State the blood parasite species.
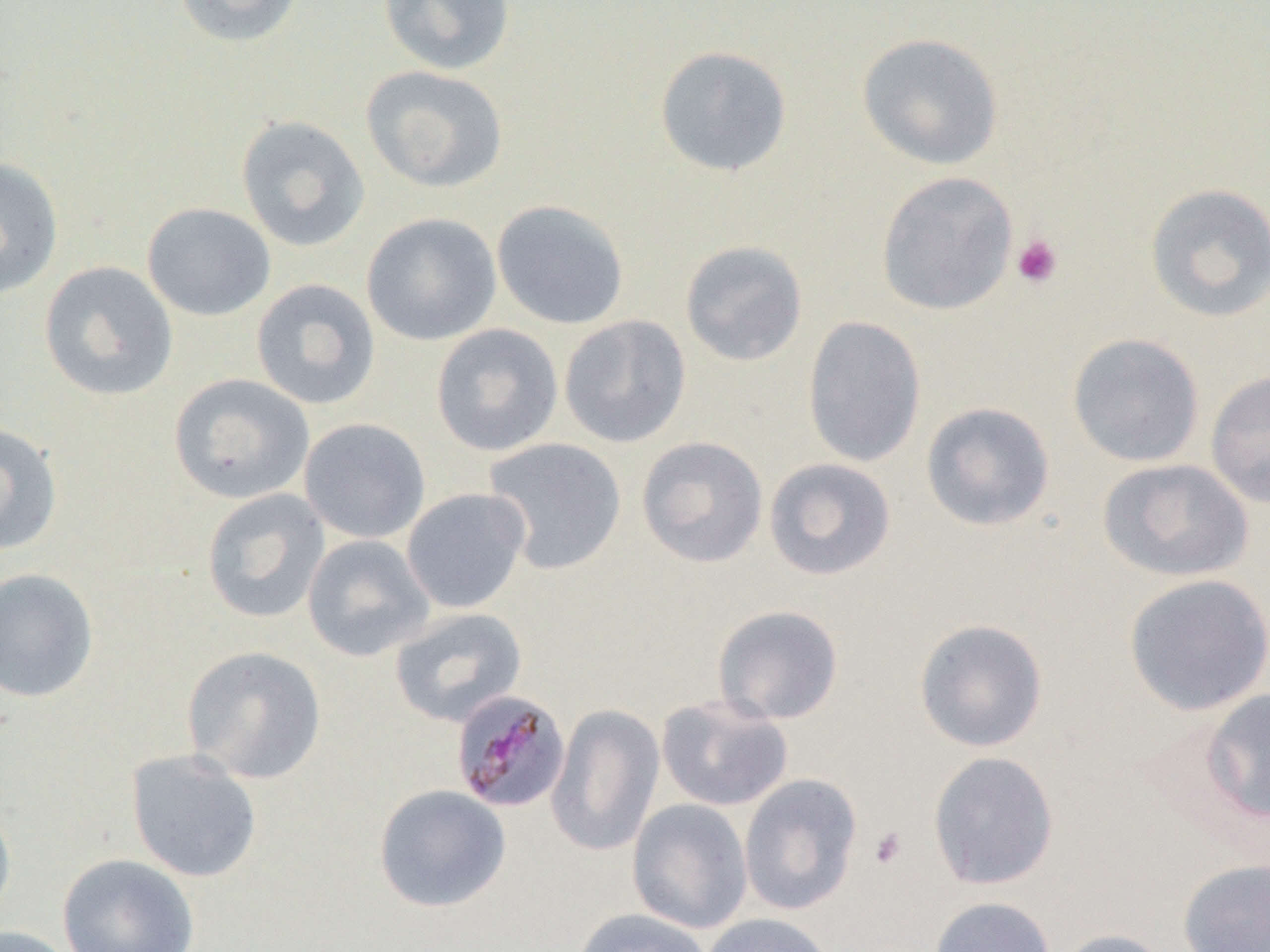
Plasmodium malariae.

Approximate bounding boxes as [x1, y1, x2, y2] in pixels. Uninfected red blood cell locations: [172, 0, 305, 48], [378, 0, 516, 75], [856, 32, 1004, 170], [654, 45, 793, 177], [361, 65, 509, 193], [235, 115, 371, 253], [0, 157, 64, 299], [876, 171, 1018, 316], [1143, 182, 1270, 323], [491, 199, 629, 330], [142, 202, 276, 322], [361, 212, 502, 346], [679, 240, 808, 367], [39, 261, 178, 401], [251, 278, 381, 411], [559, 315, 691, 448], [802, 316, 926, 468], [430, 323, 563, 457], [1067, 333, 1205, 467], [1205, 370, 1270, 509], [168, 373, 315, 505], [920, 401, 1056, 532], [298, 417, 431, 544], [0, 421, 63, 555], [636, 436, 768, 568], [482, 437, 627, 575], [763, 457, 896, 581], [1097, 458, 1254, 582], [401, 487, 531, 613], [201, 488, 331, 625], [302, 534, 435, 662], [0, 567, 99, 702], [1122, 573, 1270, 716], [712, 604, 845, 725], [389, 607, 528, 728], [913, 618, 1049, 752], [181, 645, 327, 784], [1199, 688, 1270, 825], [656, 695, 794, 812], [546, 704, 665, 857], [125, 748, 263, 883], [927, 751, 1059, 890], [739, 773, 863, 916], [374, 784, 511, 913], [0, 795, 16, 923], [626, 798, 753, 935], [56, 853, 200, 952], [1178, 859, 1270, 952], [928, 896, 1056, 952], [572, 908, 714, 952], [700, 913, 835, 952], [0, 925, 77, 952], [1051, 928, 1177, 952]. Plasmodium malariae-infected red blood cell locations: [450, 690, 571, 814]. Platelet locations: [1011, 234, 1064, 289], [869, 827, 907, 869]. Captured at 1000x magnification. Image is 1270×952 pixels. Thin blood smear. Optical microscopy. One field of a larger specimen.